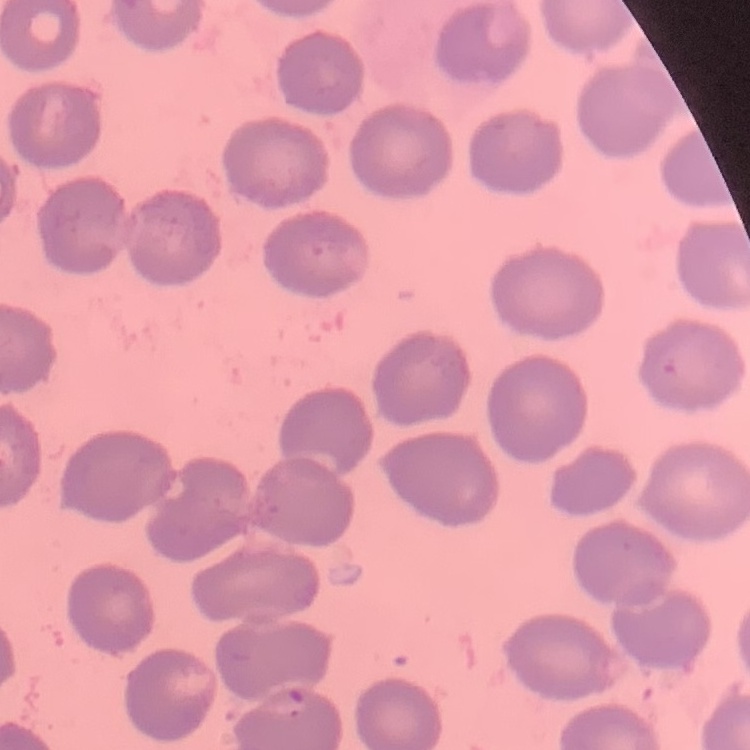
erythrocyte morphology = no rouleaux formation
preparation = thin blood smear
stain = Field's or Giemsa
image type = square crop of a larger photomicrograph